Locate every Plasmodium parasite.
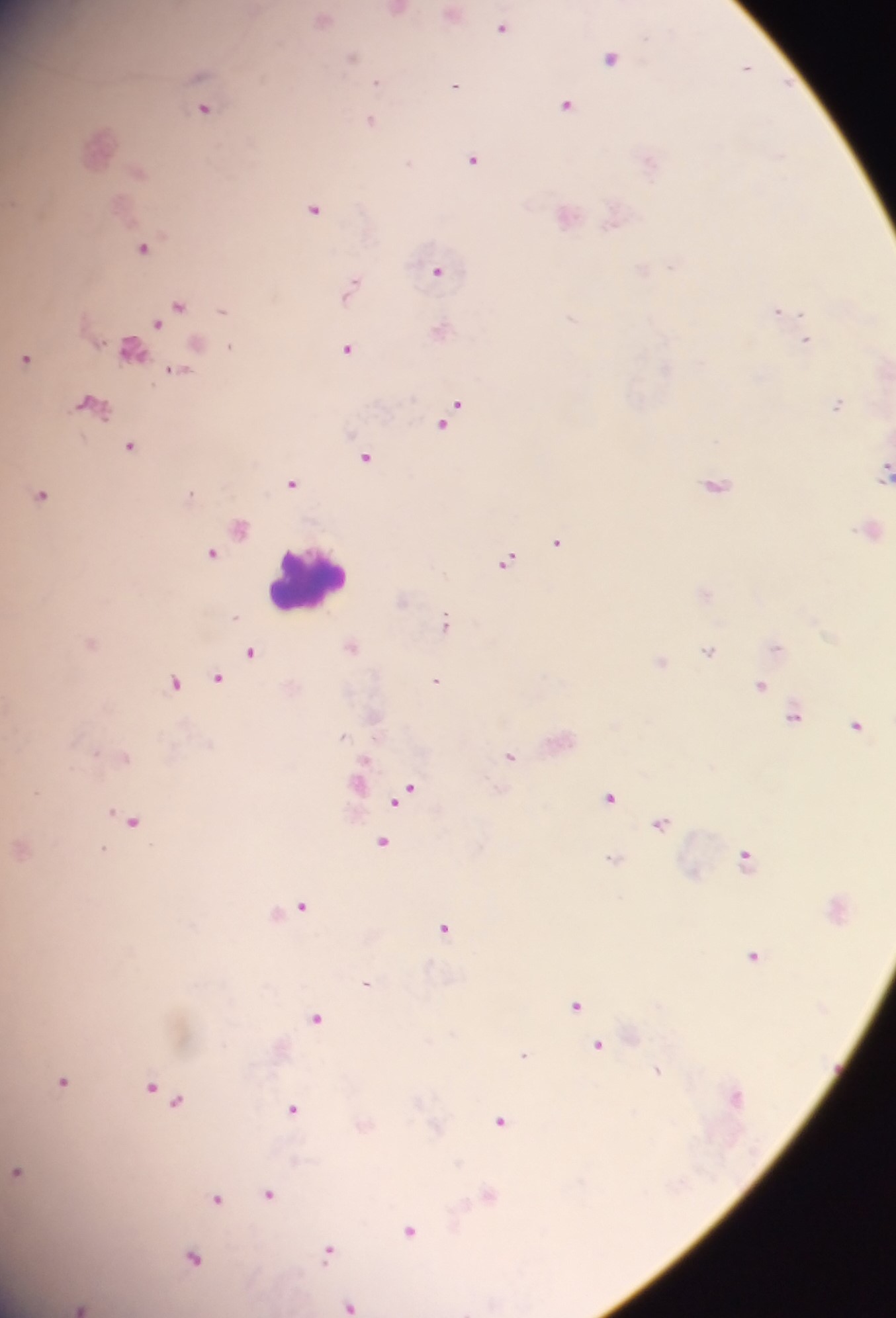
Approximate centers as x y in pixels.
Plasmodium parasites: 501 27; 350 57; 610 57; 745 66; 375 82; 454 85; 565 105; 204 110; 370 121; 779 155; 473 160; 314 209; 142 247; 437 270; 351 287; 179 305; 222 310; 777 311; 156 323; 804 341; 228 346; 131 349; 347 349; 25 358; 176 370; 89 403; 836 404; 451 413; 129 445; 365 457; 883 473; 291 483; 715 485; 190 493; 40 495; 239 528; 558 541; 210 553; 506 562; 445 623; 351 646; 776 648; 709 651; 250 652; 660 662; 216 678; 435 680; 173 683; 759 686; 793 716; 856 725; 341 736; 95 752; 510 757; 125 758; 405 793; 609 797; 129 821; 661 824; 382 842; 744 857; 611 859; 301 906; 444 928; 753 955; 365 983; 575 1006; 315 1018; 598 1046; 523 1055; 657 1070; 63 1082; 150 1088; 166 1094; 734 1096; 292 1109; 498 1121; 17 1172; 268 1194; 488 1195; 216 1200; 410 1231; 328 1251; 192 1257; 350 1305; 79 1306.

Summary:
  - Leukocyte locations: 309 579
  - Capture: mobile-phone photograph through a microscope
  - Image size: 896×1318 pixels
  - Preparation: thick blood smear
  - Field of view: single
  - Country: Ghana